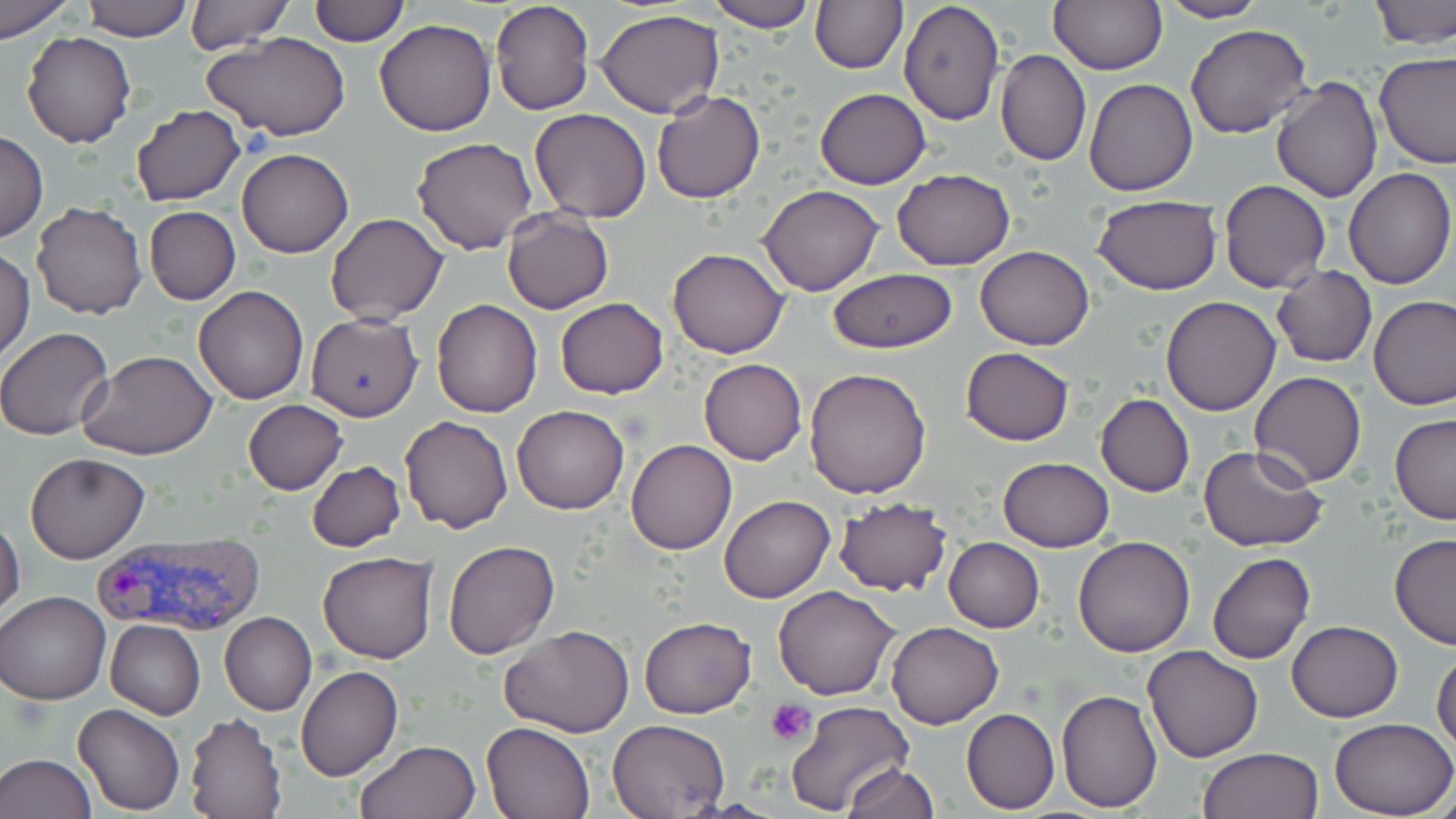
slide_level_diagnosis: Plasmodium vivax
stain: May-Grünwald-Giemsa
platelet_locations: 'approximate bounding boxes as (x1,y1)-(x2,y2) corner pairs in pixels: (765,700)-(816,748)'
magnification: 1000x
field_of_view: one of a larger specimen
preparation: thin blood film
modality: optical microscopy
plasmodium_vivax_infected_red_blood_cell_locations: 'approximate bounding boxes as (x1,y1)-(x2,y2) corner pairs in pixels: (92,533)-(264,636)'
uninfected_red_blood_cell_locations: 'approximate bounding boxes as (x1,y1)-(x2,y2) corner pairs in pixels: (0,0)-(73,40), (184,0)-(295,53), (706,0)-(820,30), (811,0)-(907,73), (1048,0)-(1165,74), (1157,0)-(1269,23), (1369,0)-(1456,49), (79,1)-(195,40), (309,1)-(408,46), (490,1)-(594,115), (898,1)-(1005,125), (595,8)-(724,117), (373,20)-(496,137), (1185,23)-(1313,139), (21,31)-(136,147), (203,31)-(350,142), (996,48)-(1092,166), (1373,52)-(1456,169), (1269,76)-(1382,203), (1083,78)-(1198,196), (816,87)-(930,188), (650,91)-(766,203), (131,105)-(246,206), (529,108)-(652,221), (0,130)-(47,243), (411,137)-(539,255), (238,148)-(353,258), (891,167)-(1015,271), (1343,167)-(1455,290), (1221,179)-(1330,294), (758,184)-(885,295), (1093,194)-(1222,294), (30,202)-(147,319), (144,207)-(240,304), (501,209)-(614,313), (325,213)-(449,326), (975,246)-(1094,349), (667,248)-(791,359), (0,249)-(35,362), (1271,266)-(1377,367), (828,268)-(958,353), (193,285)-(309,403), (1369,294)-(1456,410), (1160,295)-(1281,417), (555,297)-(668,398), (431,300)-(543,417), (304,314)-(424,421), (0,326)-(118,441), (961,348)-(1074,446), (78,350)-(218,459), (698,358)-(806,464), (804,368)-(933,498), (1250,371)-(1367,488), (1096,394)-(1195,497), (242,399)-(347,494), (511,405)-(630,514), (400,415)-(514,534), (1390,415)-(1456,524), (626,439)-(737,555), (1198,445)-(1329,552), (25,452)-(149,563), (998,458)-(1114,552), (306,461)-(406,551), (719,496)-(833,604), (832,497)-(952,597), (0,517)-(25,622), (1389,533)-(1456,650), (1074,536)-(1195,657), (944,538)-(1045,632), (442,540)-(559,658), (317,550)-(437,663), (1206,552)-(1314,665), (773,585)-(900,700), (1,590)-(110,705), (219,612)-(317,715), (639,616)-(756,719), (105,620)-(206,720), (1286,620)-(1403,721), (885,622)-(1004,729), (500,625)-(634,737), (1143,644)-(1264,762), (1433,648)-(1456,753), (295,666)-(402,781), (1056,689)-(1163,813), (784,701)-(914,818), (73,702)-(185,815), (961,708)-(1060,814), (184,713)-(285,818), (608,718)-(730,818), (1331,718)-(1456,817), (482,719)-(596,819), (356,740)-(478,819), (1197,747)-(1325,819), (0,753)-(97,819), (843,762)-(938,818)'
image_size: 1456×819 pixels